Locate every blood parasite and identify its species.
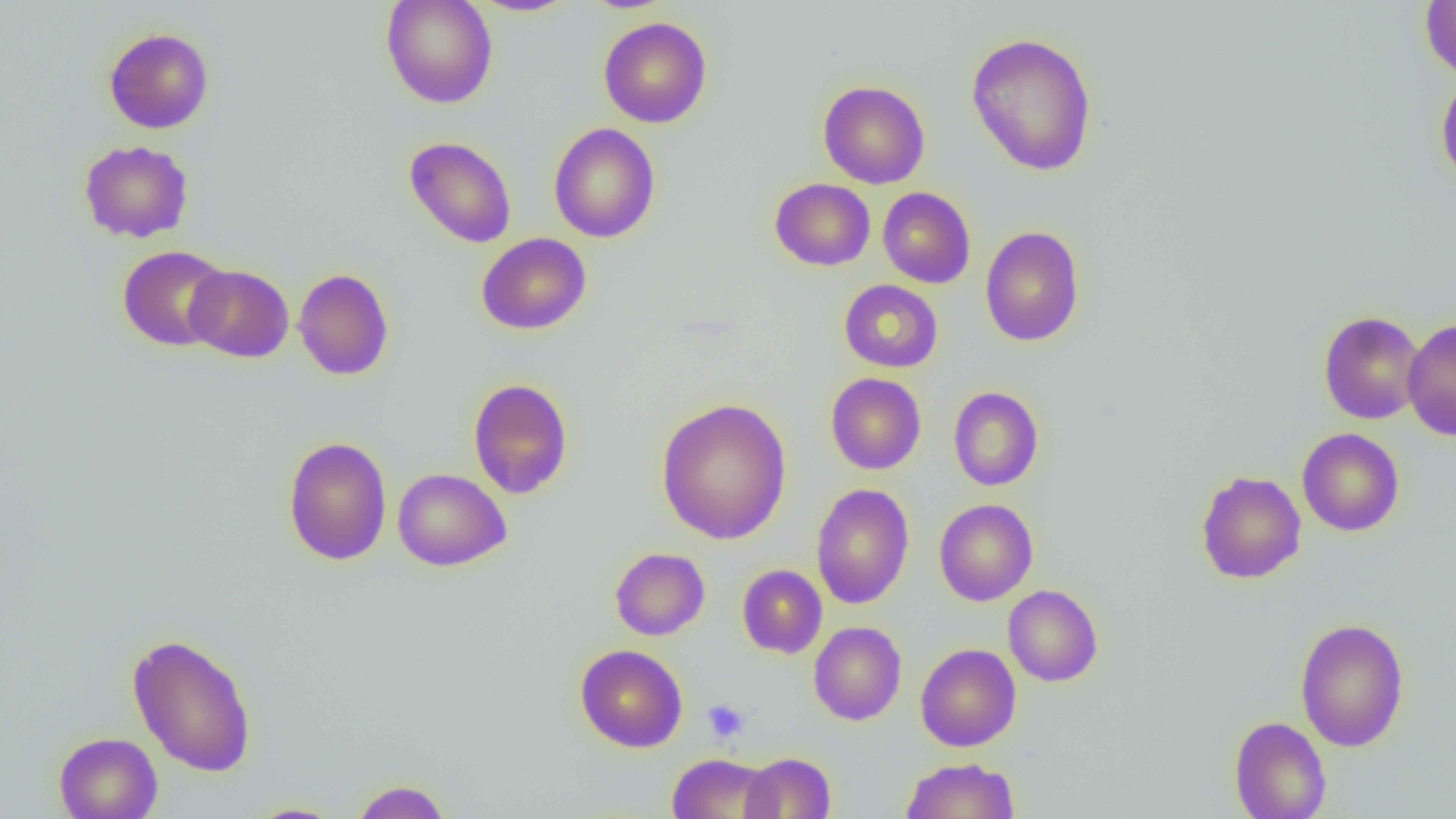
No blood parasites seen.

Approximate bounding boxes as (x1, y1, x2, y2) in pixels. Uninfected red blood cell locations: (381, 0, 498, 109), (469, 1, 580, 17), (1420, 1, 1456, 81), (598, 16, 712, 128), (103, 27, 214, 134), (966, 32, 1098, 176), (1435, 76, 1456, 191), (818, 80, 930, 189), (549, 122, 661, 243), (404, 136, 516, 247), (79, 140, 193, 243), (769, 178, 876, 271), (878, 187, 975, 288), (980, 226, 1084, 347), (476, 233, 591, 335), (117, 245, 231, 351), (184, 264, 294, 363), (293, 267, 394, 380), (836, 279, 936, 473), (839, 279, 943, 372), (1318, 310, 1426, 425), (1402, 318, 1456, 441), (825, 373, 926, 474), (468, 377, 574, 499), (948, 386, 1044, 491), (656, 398, 792, 544), (1297, 428, 1405, 536), (282, 436, 392, 565), (393, 468, 511, 571), (1195, 470, 1306, 584), (811, 484, 914, 610), (934, 499, 1038, 605), (610, 547, 710, 640), (737, 564, 827, 658), (1003, 584, 1103, 686), (1295, 618, 1409, 752), (808, 621, 906, 725), (127, 632, 257, 777), (915, 643, 1021, 751), (575, 644, 688, 752), (1229, 716, 1331, 819), (53, 732, 163, 818), (741, 752, 836, 818), (667, 753, 778, 818), (901, 757, 1020, 819), (351, 780, 452, 819), (242, 802, 348, 818). Platelet locations: (702, 699, 750, 743). Slide-level diagnosis: no evidence of blood parasites. Thin blood film. Optical microscopy. Image is 1456×819 pixels. Captured at 1000x magnification. One field of a larger specimen.